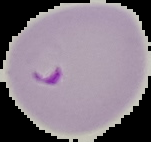
preparation = thin blood smear
image size = 151×142 pixels
image type = segmented cell region with the area outside set to black
malaria status = parasitized